Outline each Plasmodium falciparum-infected red blood cell.
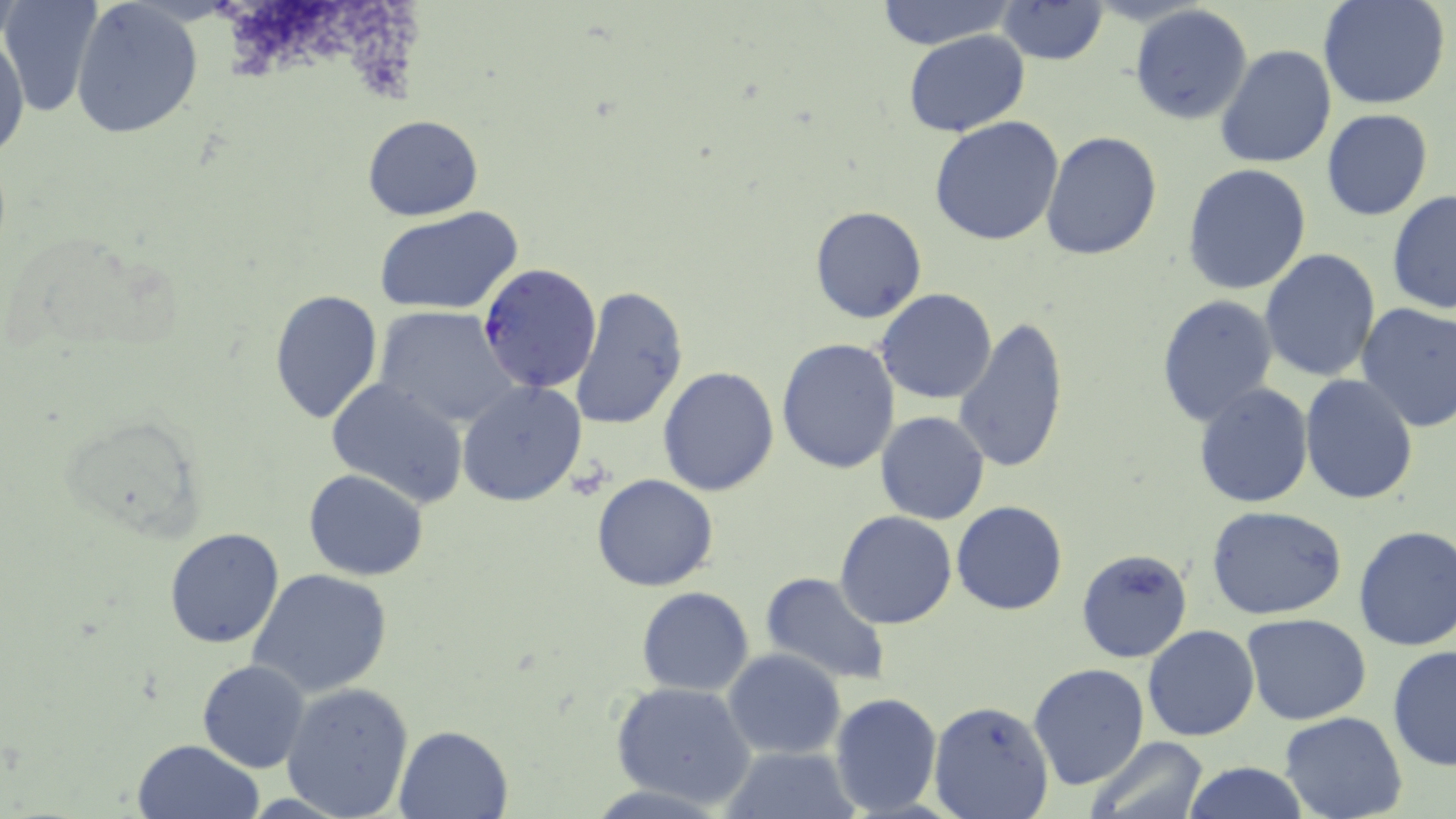
Approximate bounding boxes as named x1/y1/x2/y2 corners in pixels.
Plasmodium falciparum-infected red blood cells: (x1=477, y1=262, x2=602, y2=394).

Uninfected red blood cell locations: (x1=1, y1=0, x2=101, y2=117), (x1=872, y1=0, x2=1017, y2=50), (x1=1320, y1=0, x2=1451, y2=110), (x1=70, y1=1, x2=203, y2=139), (x1=996, y1=1, x2=1110, y2=66), (x1=1129, y1=5, x2=1254, y2=127), (x1=1, y1=26, x2=29, y2=167), (x1=903, y1=30, x2=1029, y2=137), (x1=1215, y1=42, x2=1336, y2=170), (x1=1321, y1=108, x2=1434, y2=221), (x1=361, y1=114, x2=485, y2=221), (x1=929, y1=115, x2=1064, y2=246), (x1=1042, y1=132, x2=1163, y2=261), (x1=1183, y1=164, x2=1312, y2=295), (x1=1387, y1=190, x2=1456, y2=314), (x1=809, y1=206, x2=927, y2=325), (x1=373, y1=207, x2=524, y2=316), (x1=1260, y1=248, x2=1381, y2=381), (x1=570, y1=286, x2=689, y2=432), (x1=267, y1=288, x2=384, y2=425), (x1=877, y1=288, x2=998, y2=404), (x1=1155, y1=294, x2=1280, y2=429), (x1=1355, y1=301, x2=1456, y2=433), (x1=373, y1=307, x2=518, y2=429), (x1=953, y1=315, x2=1072, y2=476), (x1=775, y1=337, x2=902, y2=474), (x1=658, y1=367, x2=781, y2=497), (x1=1299, y1=373, x2=1419, y2=505), (x1=325, y1=377, x2=470, y2=507), (x1=457, y1=381, x2=587, y2=506), (x1=1192, y1=383, x2=1314, y2=508), (x1=875, y1=411, x2=990, y2=526), (x1=303, y1=469, x2=429, y2=580), (x1=591, y1=474, x2=719, y2=592), (x1=952, y1=501, x2=1068, y2=616), (x1=1206, y1=505, x2=1349, y2=619), (x1=834, y1=511, x2=957, y2=629), (x1=1352, y1=525, x2=1456, y2=651), (x1=165, y1=527, x2=286, y2=648), (x1=1076, y1=548, x2=1193, y2=664), (x1=247, y1=568, x2=394, y2=699), (x1=759, y1=571, x2=892, y2=686), (x1=636, y1=587, x2=754, y2=696), (x1=1241, y1=612, x2=1372, y2=726), (x1=1143, y1=624, x2=1260, y2=742), (x1=1387, y1=645, x2=1456, y2=773), (x1=723, y1=650, x2=846, y2=759), (x1=197, y1=659, x2=309, y2=773), (x1=1026, y1=663, x2=1150, y2=792), (x1=609, y1=681, x2=755, y2=808), (x1=280, y1=682, x2=416, y2=818), (x1=829, y1=691, x2=942, y2=814), (x1=928, y1=700, x2=1054, y2=819), (x1=1277, y1=712, x2=1407, y2=819), (x1=393, y1=725, x2=512, y2=818), (x1=1087, y1=737, x2=1209, y2=819), (x1=134, y1=739, x2=261, y2=819), (x1=719, y1=745, x2=860, y2=819), (x1=1182, y1=760, x2=1309, y2=819). Slide-level diagnosis: Plasmodium falciparum. Single field of view. Thin blood film. 1000x magnification. May-Grünwald-Giemsa-stained preparation. Light microscopy. Image is 1456×819 pixels.